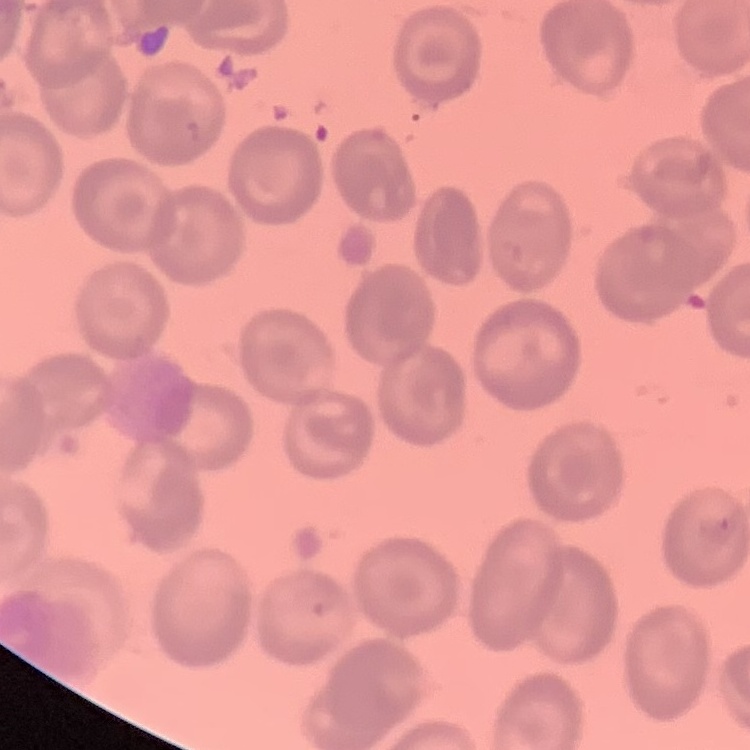 The erythrocytes exhibit no rouleaux formation. Field's or Giemsa stain. Square crop of a larger photomicrograph. Thin blood film.